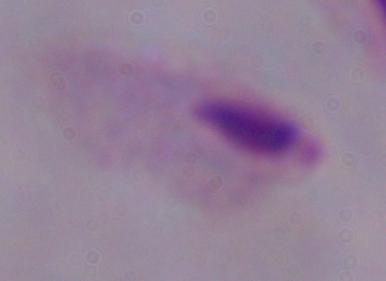

Summary:
  - Modality: micrograph
  - Identification: trichomonad
  - Magnification: 1000x